Assess this cell for malaria.
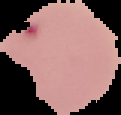

It is parasitized.

image type = segmented cell region with the area outside set to black
preparation = thin blood smear
image size = 121×115 pixels